Name the cell type shown.
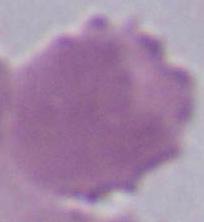
An erythrocyte.

magnification = 1000x
modality = micrograph